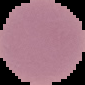
Summary:
  - Image type: segmented cell region on a black background
  - Image size: 85×85 pixels
  - Result: no malaria parasites detected
  - Preparation: thin blood smear